State the blood parasite species.
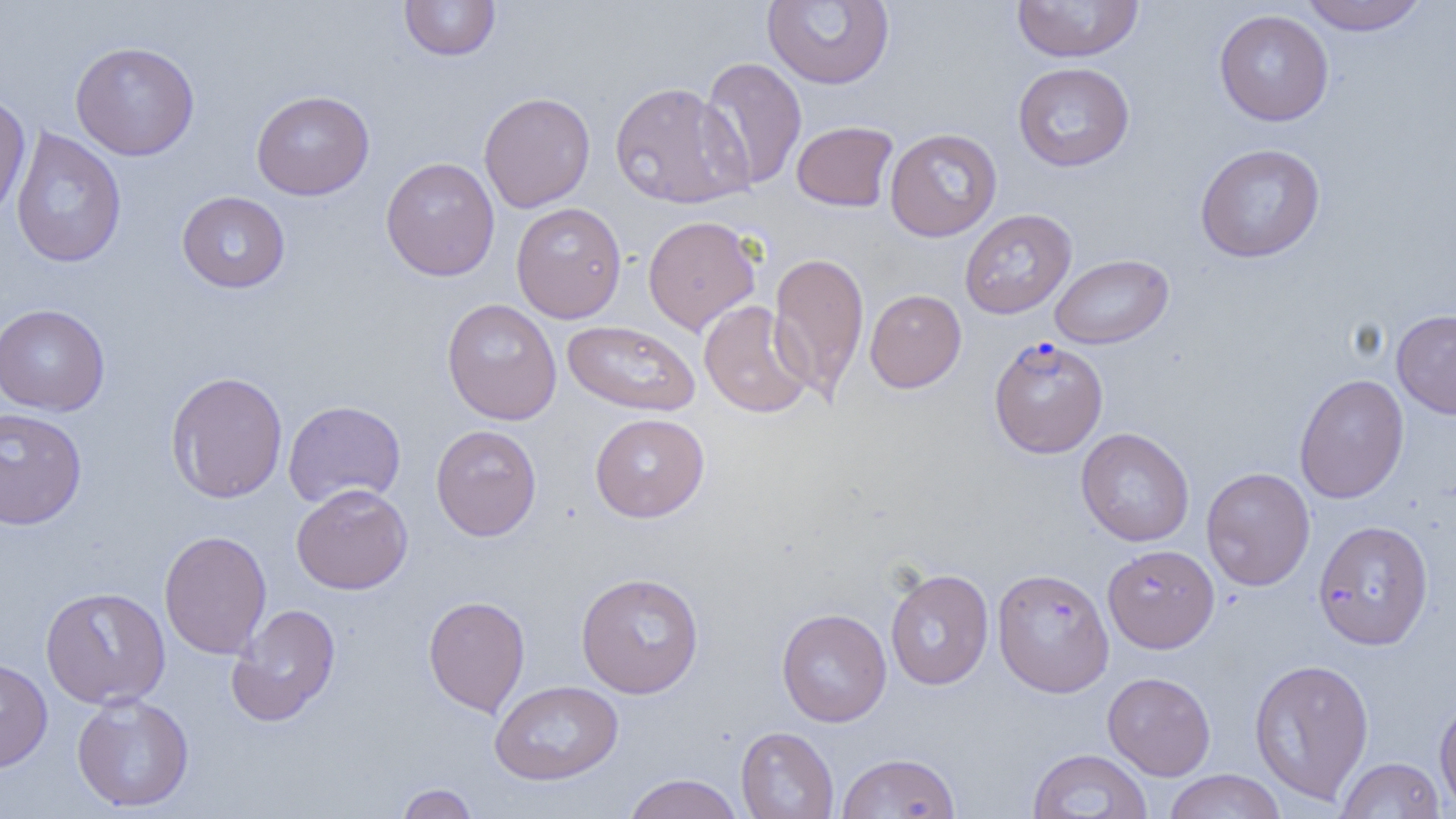
Plasmodium falciparum.

image size = 1456×819 pixels
uninfected red blood cell locations = approximate bounding boxes as (x1,y1)-(x2,y2) corner pairs in pixels: (399,0)-(501,61), (762,0)-(895,89), (1297,0)-(1430,36), (1011,1)-(1145,63), (1214,9)-(1333,126), (70,41)-(200,160), (698,56)-(808,191), (1013,62)-(1135,172), (609,81)-(751,209), (251,90)-(375,200), (479,91)-(596,213), (0,92)-(31,222), (792,120)-(899,212), (10,127)-(126,268), (885,128)-(1002,242), (1194,143)-(1326,263), (380,157)-(500,281), (177,191)-(290,293), (511,202)-(626,323), (960,208)-(1076,319), (643,215)-(761,335), (768,251)-(870,400), (1050,253)-(1174,349), (861,297)-(962,401), (441,298)-(562,425), (699,300)-(813,418), (0,303)-(110,416), (1392,310)-(1456,419), (562,320)-(701,417), (166,371)-(288,503), (1294,374)-(1409,503), (283,400)-(406,508), (0,407)-(87,530), (590,413)-(710,522), (430,424)-(542,541), (1076,427)-(1195,546), (1201,467)-(1315,591), (291,483)-(413,594), (1313,519)-(1433,650), (158,530)-(272,659), (1102,544)-(1220,653), (992,567)-(1114,697), (885,568)-(994,690), (576,571)-(705,698), (40,586)-(170,708), (423,595)-(530,718), (226,603)-(342,726), (776,608)-(892,727), (0,658)-(53,772), (1249,658)-(1375,805), (1102,672)-(1216,780), (490,680)-(623,785), (71,692)-(194,813), (1434,697)-(1456,815), (735,726)-(839,819), (1027,749)-(1153,818), (837,752)-(961,818), (1336,757)-(1446,818), (1164,769)-(1286,819), (622,773)-(745,819), (395,783)-(480,818)
magnification = 1000x
modality = light microscopy
Plasmodium falciparum-infected red blood cell locations = approximate bounding boxes as (x1,y1)-(x2,y2) corner pairs in pixels: (989,336)-(1108,458)
field of view = single
preparation = thin blood film